Classify this cell by malaria status.
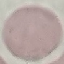
It is uninfected.

Summary:
  - Preparation: thin blood smear
  - Capture: smartphone through the microscope eyepiece
  - Stain: Giemsa
  - Image type: automatically extracted cell patch, resized to 64 × 64 pixels